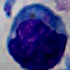
A white blood cell is shown. Captured at 1000x magnification. Photomicrograph.